Report the malaria status of this cell.
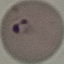
Parasitized.

preparation: thin blood smear
stain: Giemsa
capture: smartphone through the microscope eyepiece
image_type: automatically extracted cell patch, resized to 64 × 64 pixels